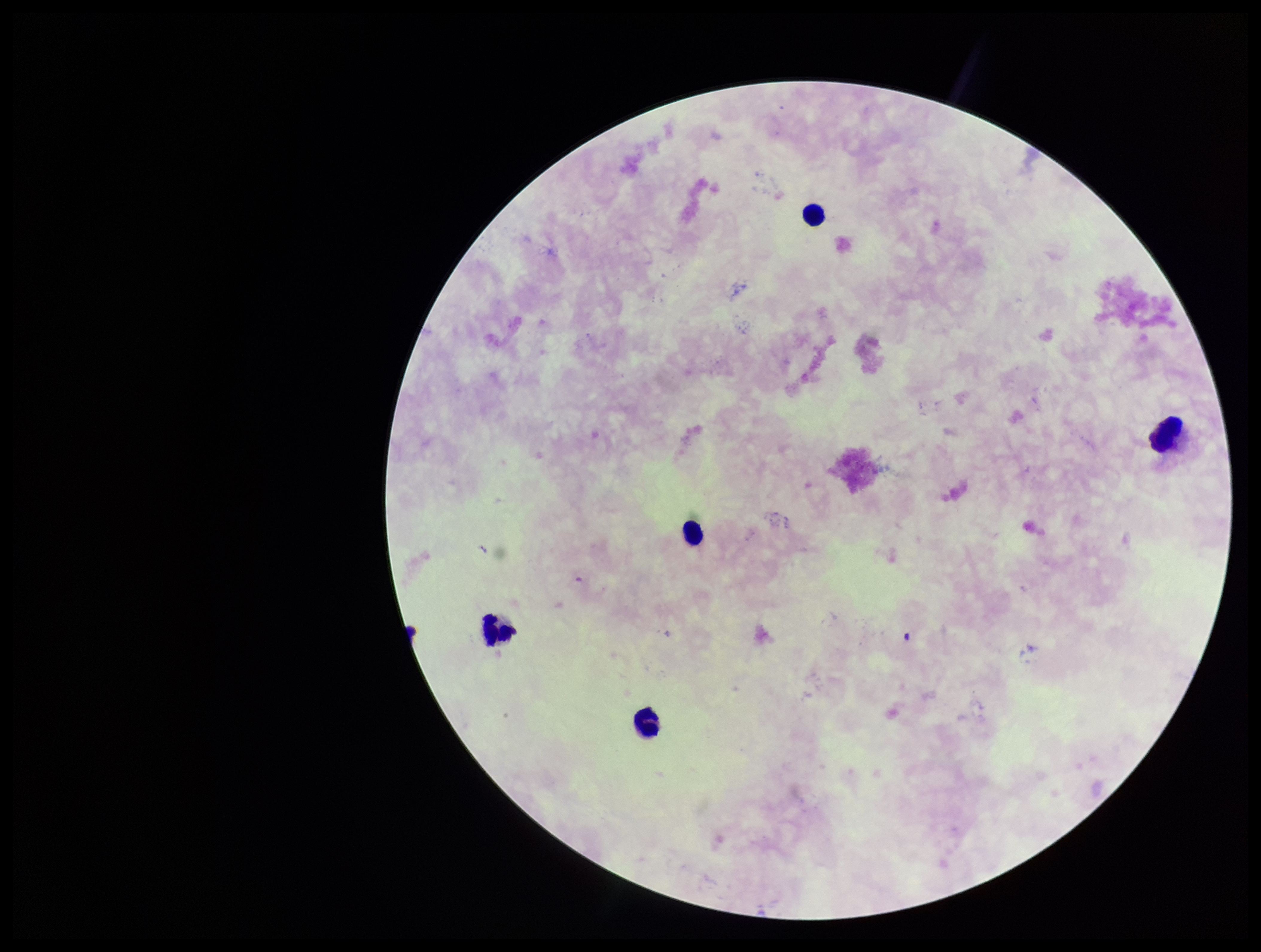
stain: Giemsa
leukocyte_count: 5
parasite_count: 0
image_size: 1261×952 pixels
patient_malaria_status: negative
plasmodium_parasites: none detected
field_of_view: single
preparation: thick smear
capture: smartphone photograph through the microscope eyepiece